State which parasite is depicted.
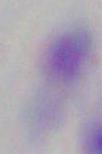

Toxoplasma gondii.

1000x magnification. Micrograph.